Identify the preparation type.
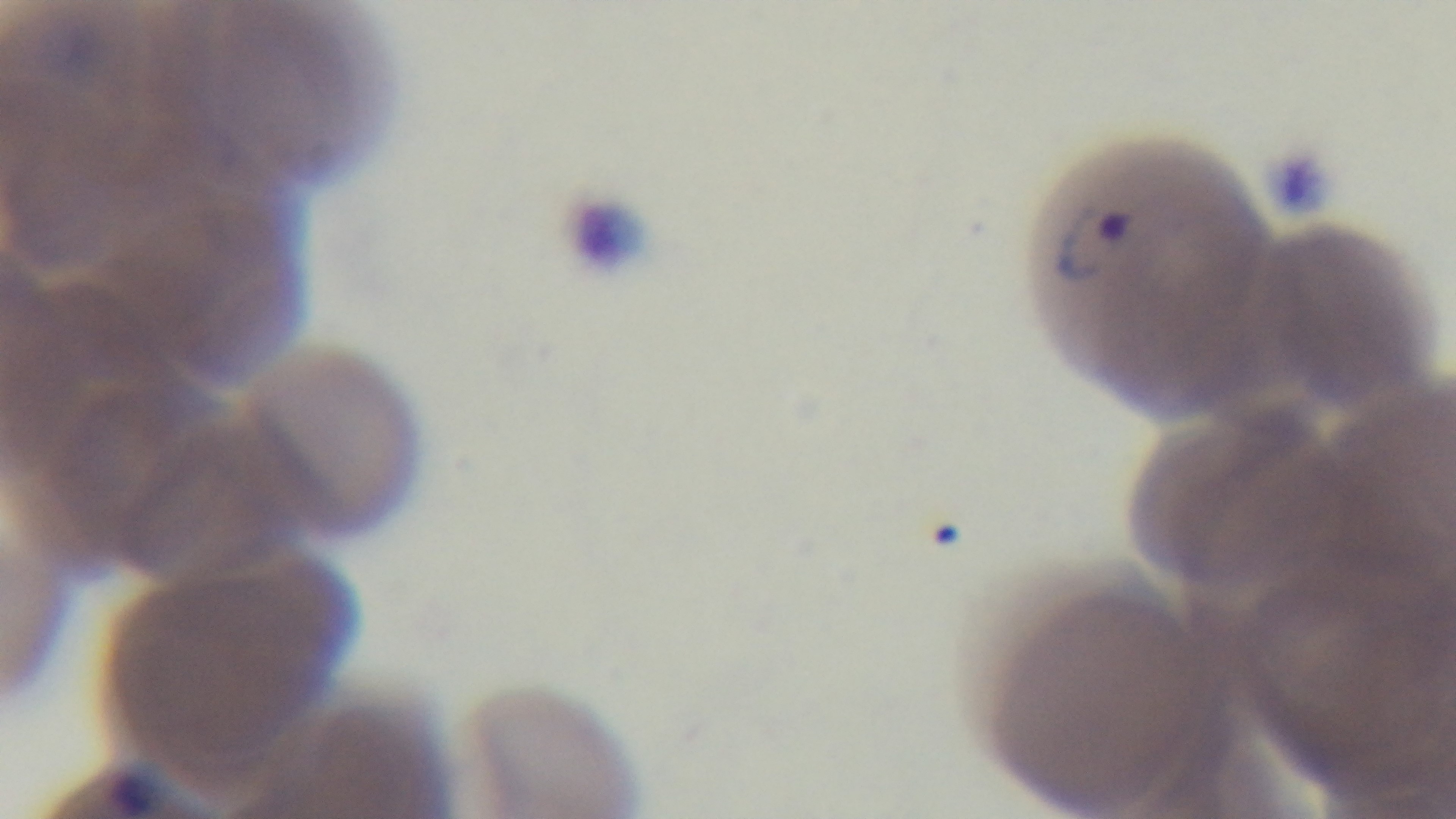

It is a thin blood film.

malaria status = infected
objective = 100x oil immersion
stain = Giemsa
capture = mounted 4K digital camera
modality = light microscopy
field of view = one from the slide